Draw a bounding box around every malaria parasite, every leukocyte, and every artifact (stain precipitate or debris).
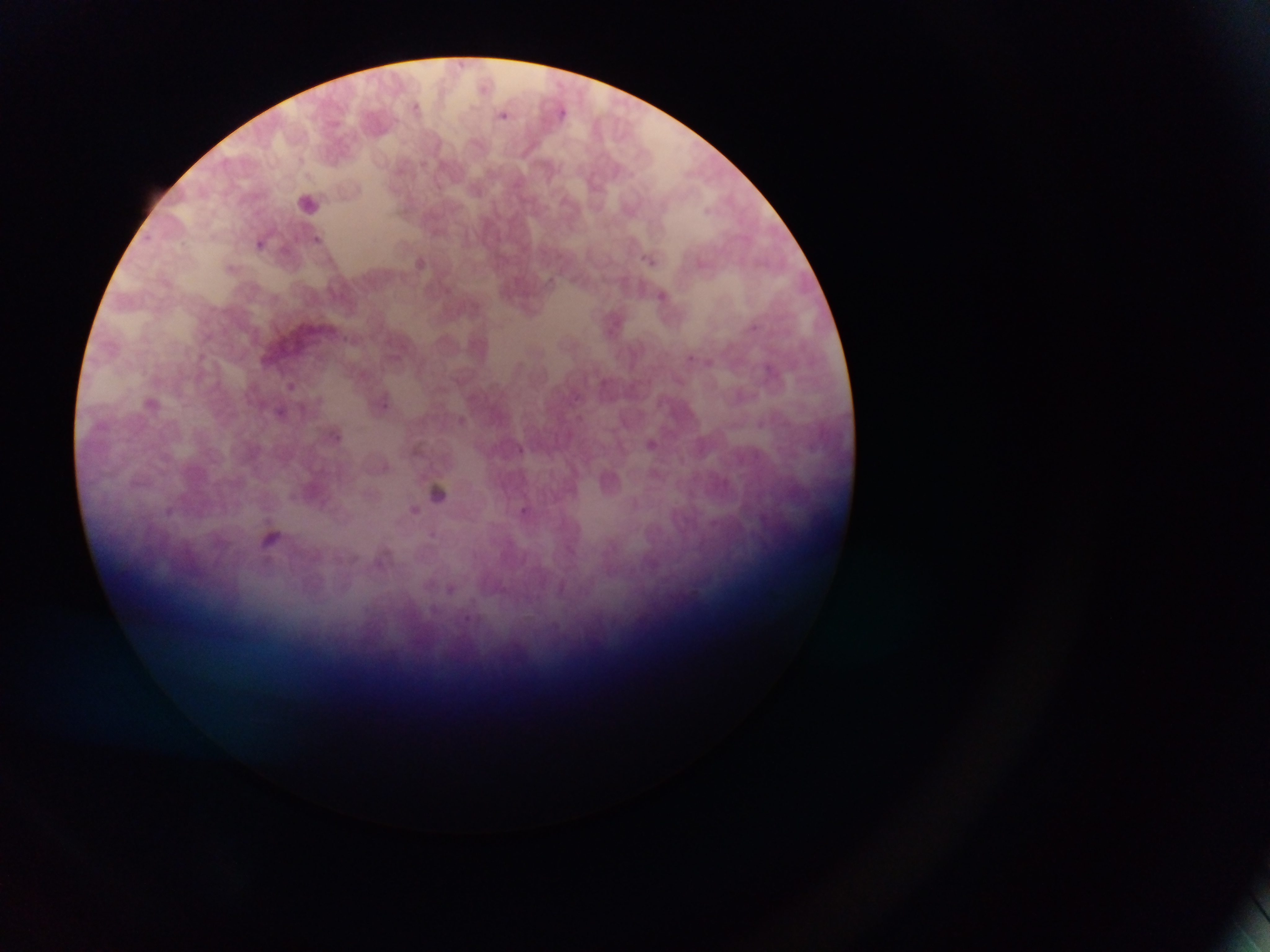

Approximate bounding boxes as (left, top, right, bottom) in pixels.
Malaria parasites: (411, 98, 443, 126), (503, 111, 523, 124), (564, 112, 580, 124), (310, 233, 327, 252), (258, 238, 272, 256), (640, 251, 663, 270), (654, 285, 676, 314), (745, 320, 760, 336), (684, 350, 695, 364), (288, 375, 310, 397), (377, 392, 399, 413), (266, 403, 305, 424), (574, 411, 598, 439), (326, 426, 349, 451), (514, 445, 536, 468), (515, 503, 533, 522), (427, 527, 450, 545), (270, 530, 282, 540).
No leukocytes observed.

Summary:
  - Capture: mobile-phone photograph through a microscope
  - Preparation: thin blood film
  - Image size: 1270×952 pixels
  - Field of view: single
  - Country: Ghana